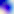

Captured at 400x magnification. Photomicrograph. Toxoplasma gondii is seen.